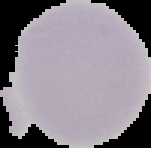

Summary:
  - Image size: 151×148 pixels
  - Preparation: thin blood smear
  - Malaria status: uninfected
  - Image type: cell region segmented out of the field of view; surrounding area masked to black